Identify the parasite.
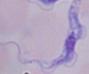

A trypanosome.

Summary:
  - Magnification: 1000x
  - Modality: micrograph